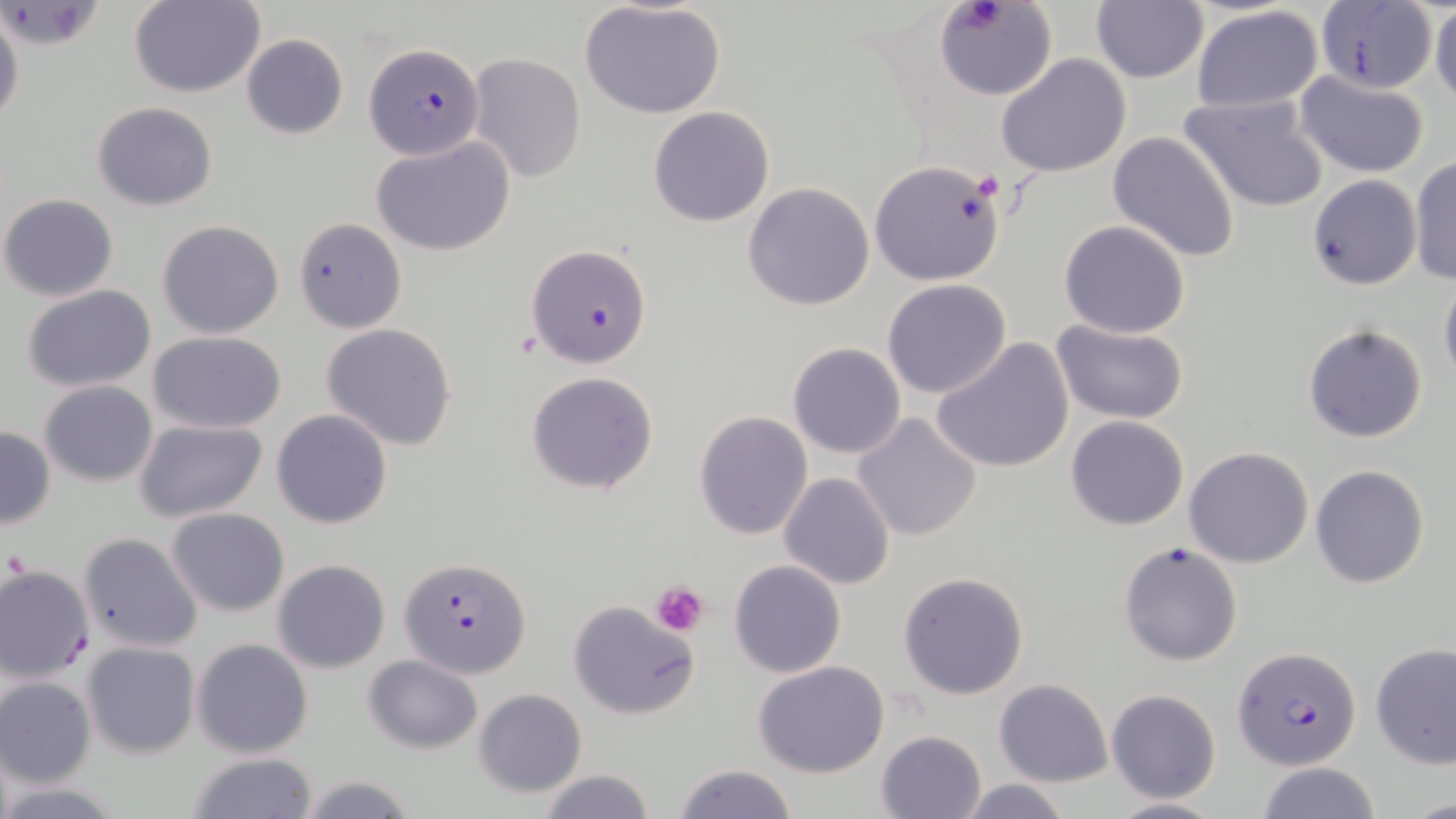
slide-level diagnosis = Plasmodium falciparum
stain = May-Grünwald-Giemsa
Plasmodium falciparum-infected red blood cell locations = approximate bounding boxes as named x1/y1/x2/y2 corners in pixels: (x1=363, y1=42, x2=484, y2=160), (x1=527, y1=243, x2=652, y2=370), (x1=400, y1=557, x2=532, y2=678), (x1=1234, y1=646, x2=1360, y2=770)
uninfected red blood cell locations = approximate bounding boxes as named x1/y1/x2/y2 corners in pixels: (x1=935, y1=0, x2=1056, y2=100), (x1=130, y1=1, x2=265, y2=98), (x1=578, y1=1, x2=727, y2=120), (x1=1090, y1=2, x2=1209, y2=84), (x1=1308, y1=4, x2=1442, y2=92), (x1=1190, y1=5, x2=1325, y2=115), (x1=1429, y1=5, x2=1455, y2=107), (x1=0, y1=7, x2=24, y2=129), (x1=241, y1=34, x2=348, y2=140), (x1=468, y1=53, x2=586, y2=183), (x1=996, y1=53, x2=1132, y2=177), (x1=1295, y1=72, x2=1431, y2=179), (x1=1180, y1=92, x2=1329, y2=214), (x1=93, y1=102, x2=218, y2=210), (x1=648, y1=105, x2=776, y2=227), (x1=1107, y1=129, x2=1241, y2=263), (x1=372, y1=136, x2=518, y2=257), (x1=1408, y1=154, x2=1456, y2=286), (x1=869, y1=159, x2=1007, y2=286), (x1=1307, y1=174, x2=1420, y2=290), (x1=743, y1=182, x2=875, y2=311), (x1=0, y1=193, x2=119, y2=301), (x1=295, y1=217, x2=407, y2=335), (x1=157, y1=219, x2=285, y2=339), (x1=1058, y1=220, x2=1190, y2=338), (x1=1439, y1=273, x2=1456, y2=393), (x1=882, y1=279, x2=1013, y2=399), (x1=22, y1=284, x2=157, y2=392), (x1=1050, y1=320, x2=1189, y2=422), (x1=321, y1=322, x2=458, y2=451), (x1=1303, y1=322, x2=1430, y2=444), (x1=148, y1=331, x2=289, y2=435), (x1=932, y1=335, x2=1076, y2=473), (x1=788, y1=342, x2=906, y2=459), (x1=525, y1=371, x2=659, y2=495), (x1=40, y1=380, x2=157, y2=487), (x1=272, y1=408, x2=393, y2=529), (x1=693, y1=410, x2=814, y2=539), (x1=852, y1=411, x2=984, y2=541), (x1=1065, y1=415, x2=1189, y2=531), (x1=136, y1=419, x2=268, y2=524), (x1=0, y1=425, x2=56, y2=529), (x1=1184, y1=446, x2=1313, y2=568), (x1=1309, y1=463, x2=1431, y2=589), (x1=778, y1=473, x2=894, y2=590), (x1=166, y1=506, x2=289, y2=616), (x1=77, y1=532, x2=204, y2=653), (x1=1117, y1=540, x2=1242, y2=667), (x1=272, y1=559, x2=391, y2=674), (x1=728, y1=559, x2=848, y2=678), (x1=0, y1=565, x2=97, y2=683), (x1=898, y1=569, x2=1030, y2=700), (x1=567, y1=599, x2=699, y2=720), (x1=191, y1=637, x2=314, y2=758), (x1=82, y1=641, x2=200, y2=758), (x1=1370, y1=644, x2=1456, y2=769), (x1=363, y1=655, x2=482, y2=754), (x1=753, y1=660, x2=889, y2=778), (x1=1, y1=676, x2=97, y2=789), (x1=993, y1=679, x2=1112, y2=787), (x1=473, y1=688, x2=588, y2=797), (x1=1106, y1=688, x2=1221, y2=803), (x1=876, y1=730, x2=985, y2=817), (x1=183, y1=752, x2=320, y2=819), (x1=1255, y1=761, x2=1383, y2=818), (x1=672, y1=763, x2=800, y2=819), (x1=537, y1=770, x2=656, y2=819), (x1=297, y1=773, x2=420, y2=819), (x1=955, y1=777, x2=1075, y2=819), (x1=1107, y1=795, x2=1227, y2=818)
field of view = single
platelet locations = approximate bounding boxes as named x1/y1/x2/y2 corners in pixels: (x1=954, y1=2, x2=1011, y2=34), (x1=974, y1=172, x2=1004, y2=201), (x1=5, y1=551, x2=31, y2=584), (x1=651, y1=580, x2=709, y2=636)
preparation = thin blood film
modality = light microscopy
image size = 1456×819 pixels
magnification = 1000x